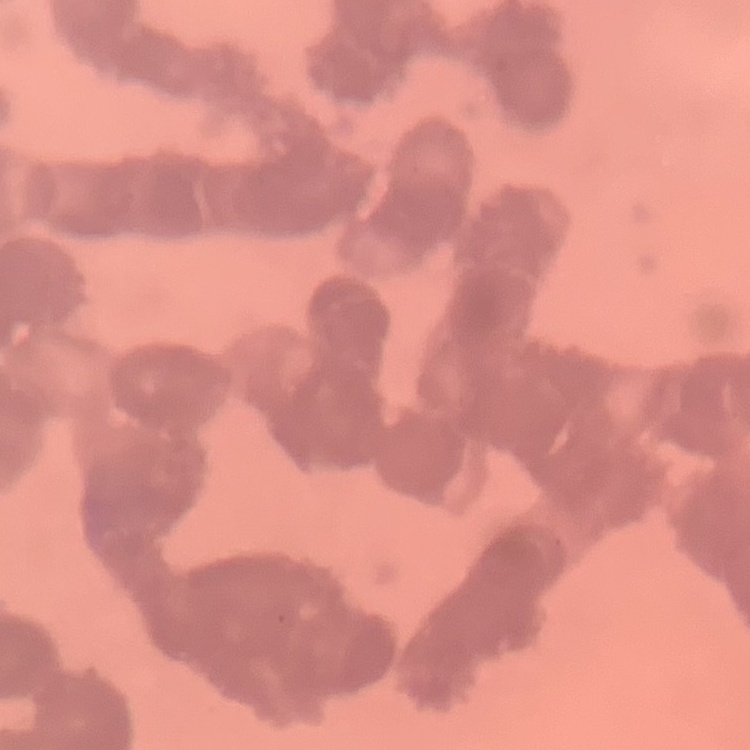
red blood cell morphology = rouleaux formation
stain = Field's or Giemsa
image type = one tile cut from a larger photomicrograph
preparation = thin peripheral smear